State the blood parasite species.
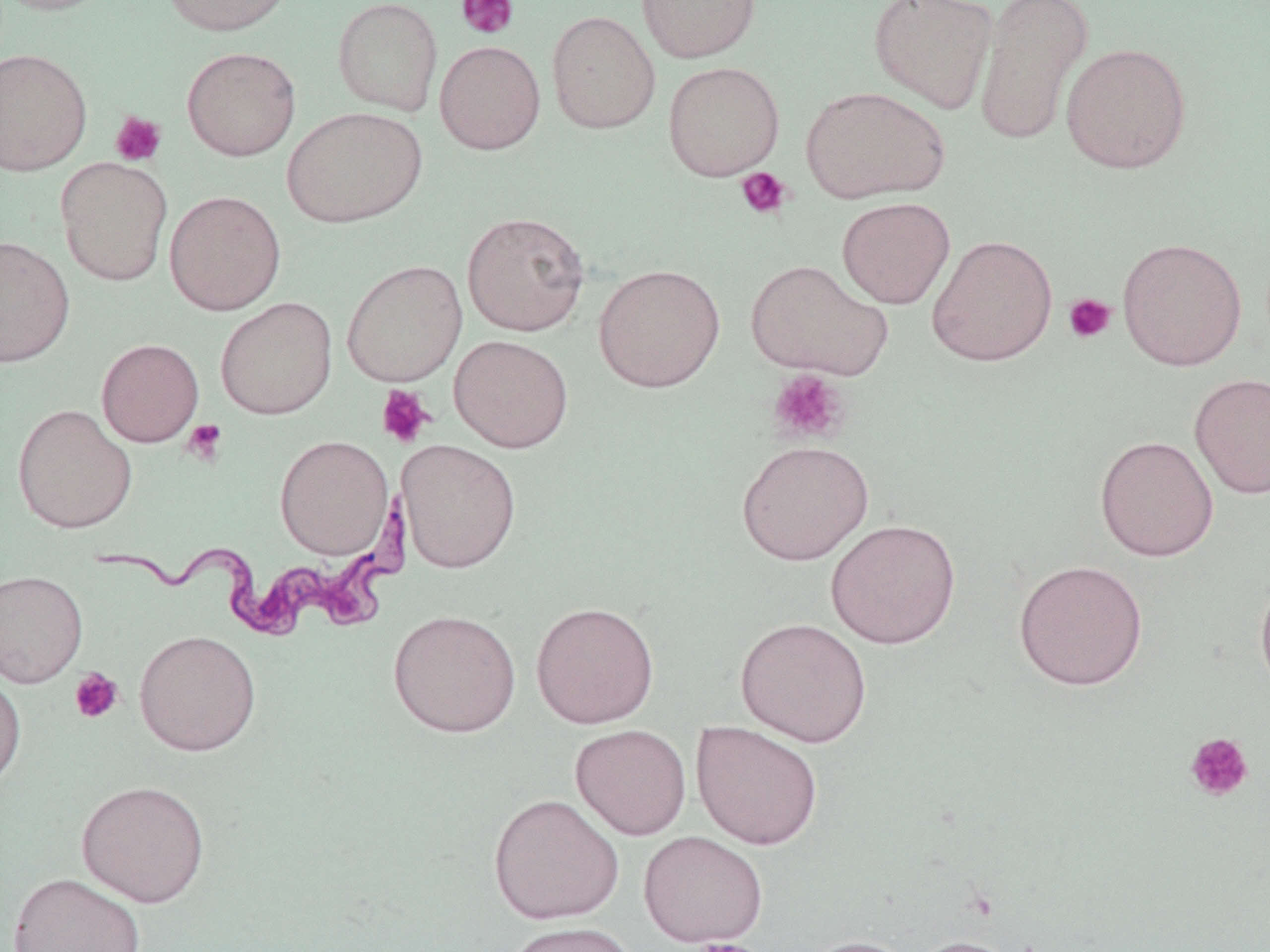

Trypanosoma brucei.

Approximate bounding boxes as (x1,y1)-(x2,y2) corner pairs in pixels. Uninfected red blood cell locations: (0,0)-(118,16), (159,0)-(297,36), (333,0)-(443,116), (636,0)-(760,64), (868,0)-(998,114), (973,0)-(1094,146), (546,11)-(661,134), (434,40)-(545,154), (1060,42)-(1192,174), (181,46)-(301,161), (0,48)-(93,176), (662,61)-(784,180), (800,86)-(950,203), (281,106)-(427,228), (55,156)-(173,286), (164,190)-(286,316), (836,196)-(955,309), (461,211)-(590,336), (926,234)-(1058,367), (0,235)-(75,368), (1117,237)-(1247,371), (745,258)-(893,380), (341,259)-(467,387), (593,263)-(725,393), (215,297)-(337,419), (449,334)-(573,452), (96,338)-(204,447), (1189,372)-(1270,499), (12,404)-(137,534), (274,434)-(394,559), (1094,434)-(1219,561), (396,439)-(521,573), (736,439)-(873,565), (825,518)-(961,649), (1013,558)-(1148,691), (0,569)-(87,687), (1255,569)-(1270,698), (530,600)-(659,729), (388,609)-(521,737), (735,616)-(872,748), (134,629)-(261,756), (0,670)-(26,794), (691,721)-(824,850), (570,724)-(691,840), (76,779)-(210,908), (488,792)-(624,924), (638,830)-(768,948), (7,872)-(147,952), (502,921)-(641,952), (798,935)-(917,952), (908,935)-(1024,952). Platelet locations: (456,0)-(519,39), (110,111)-(167,167), (736,167)-(793,220), (1062,293)-(1116,344), (766,369)-(851,446), (376,384)-(435,448), (182,419)-(228,465), (69,668)-(124,724), (1185,732)-(1255,803), (684,938)-(767,952). Trypanosoma brucei locations: (94,482)-(394,636). Thin blood film. May-Grünwald-Giemsa stain. One field of a larger specimen. Image is 1270×952 pixels. Captured at 1000x magnification. Optical microscopy.